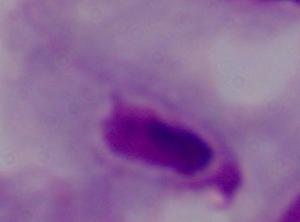
Summary:
  - Modality: micrograph
  - Identification: trichomonad
  - Magnification: 1000x